Give the position of every malaria parasite.
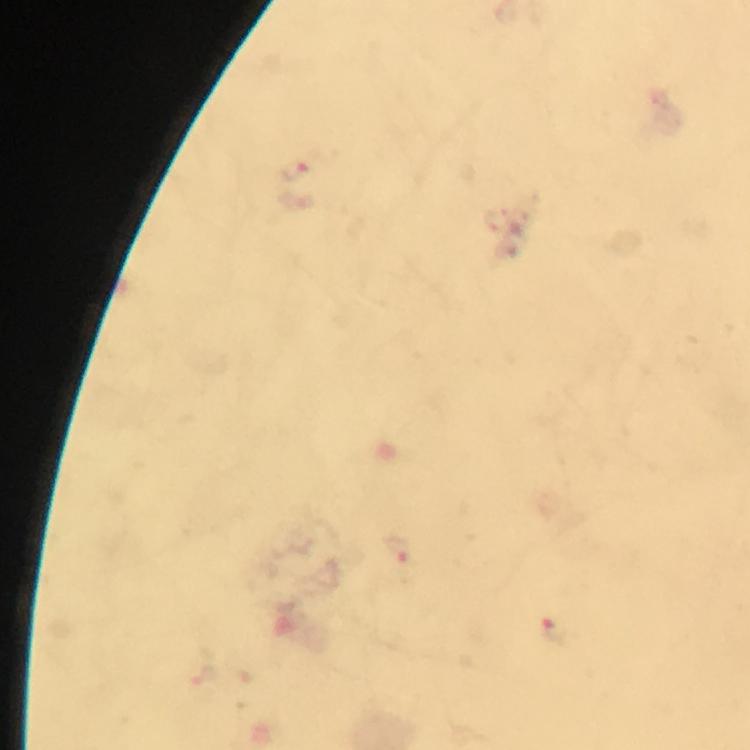

Approximate object centers, in pixels from the top-left corner.
Malaria parasites: (x=296, y=172), (x=398, y=551), (x=554, y=631).

Summary:
  - Cropped from: a single field of view
  - Preparation: thick blood smear
  - Capture: smartphone mounted on the microscope
  - Stain: Giemsa
  - Immersion oil: used
  - Magnification: 100x
  - Context: from a diagnostic examination for malaria
  - Image size: 750×750 pixels